State the preparation type.
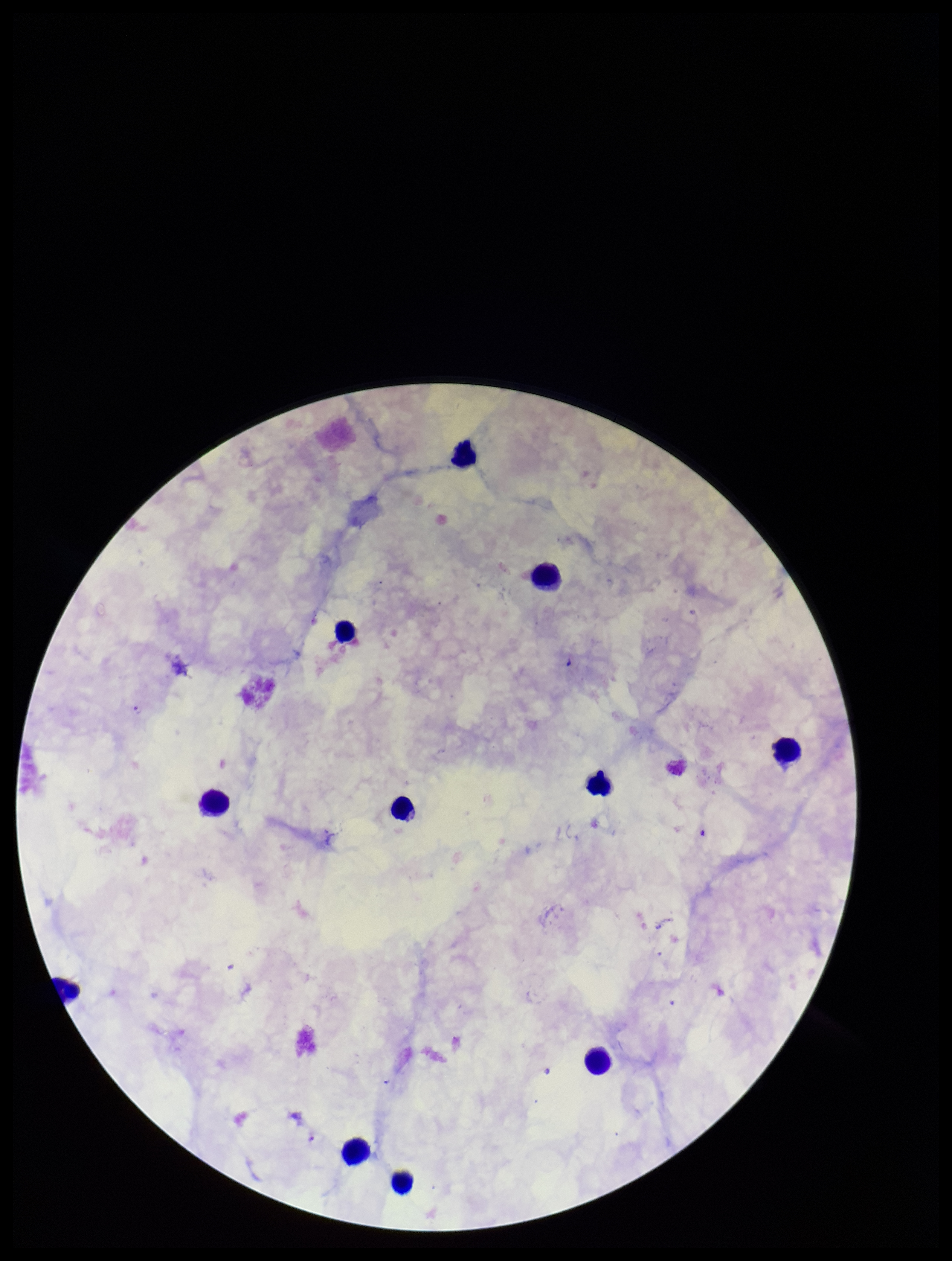

Thick.

Summary:
  - Capture: smartphone photograph through the microscope eyepiece
  - Image size: 952×1261 pixels
  - Parasite count: 1
  - Patient malaria status: infected
  - Species reported for this patient: Plasmodium falciparum
  - Stain: Giemsa
  - Field of view: one from this slide
  - Leukocyte count: 11
  - Plasmodium parasites: identified